Give the extent of all uninfected red blood cells.
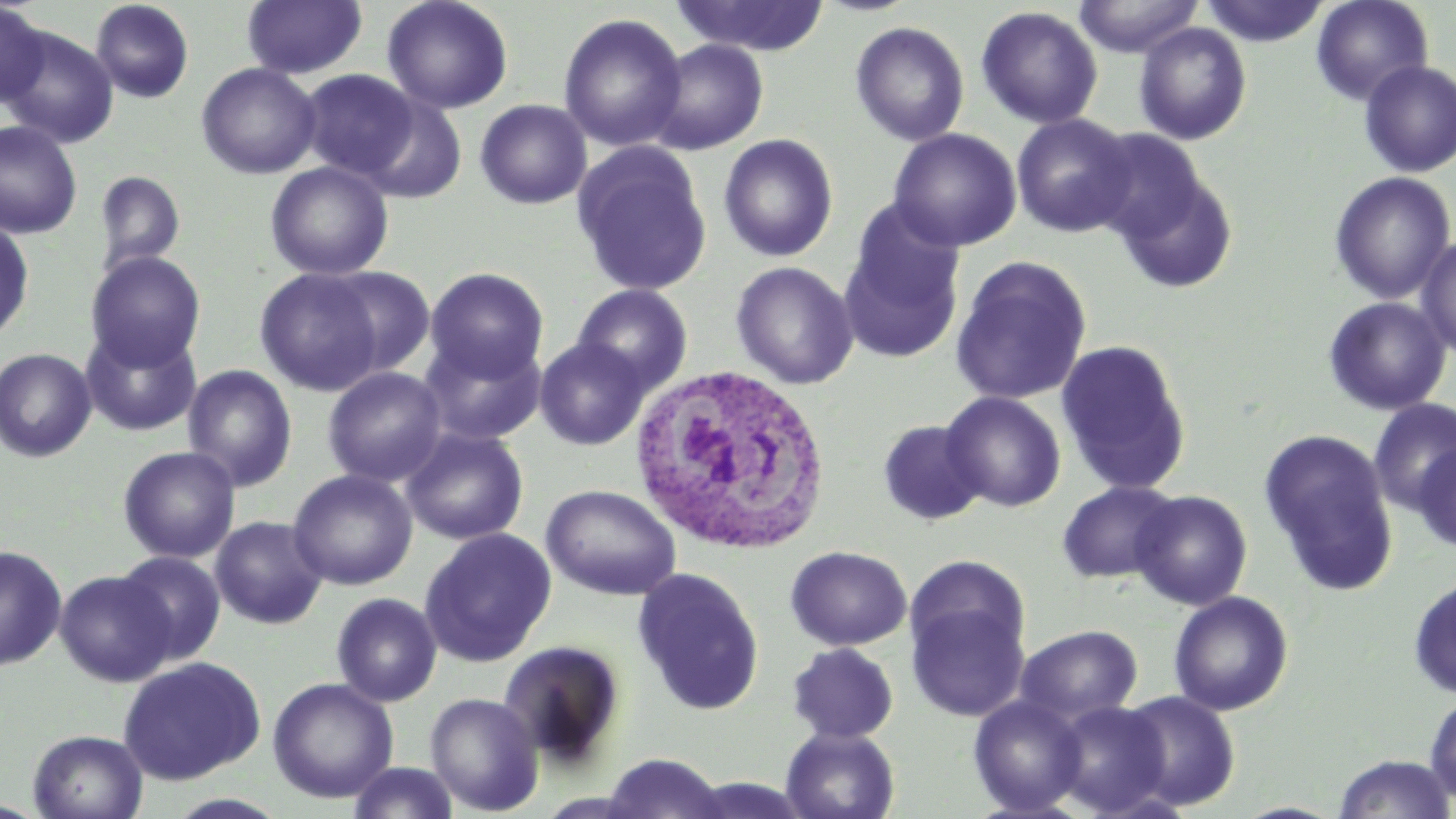

Approximate bounding boxes as named x1/y1/x2/y2 corners in pixels.
Uninfected red blood cells: (x1=90, y1=0, x2=194, y2=103), (x1=241, y1=0, x2=367, y2=80), (x1=382, y1=0, x2=514, y2=114), (x1=669, y1=0, x2=831, y2=56), (x1=1072, y1=0, x2=1204, y2=58), (x1=1199, y1=0, x2=1331, y2=47), (x1=1310, y1=0, x2=1434, y2=106), (x1=0, y1=1, x2=49, y2=108), (x1=975, y1=6, x2=1103, y2=129), (x1=558, y1=13, x2=687, y2=151), (x1=849, y1=21, x2=970, y2=146), (x1=1133, y1=22, x2=1252, y2=145), (x1=1, y1=26, x2=119, y2=148), (x1=648, y1=38, x2=770, y2=155), (x1=1358, y1=60, x2=1456, y2=178), (x1=196, y1=62, x2=322, y2=179), (x1=299, y1=69, x2=419, y2=179), (x1=356, y1=94, x2=468, y2=204), (x1=475, y1=99, x2=592, y2=209), (x1=1011, y1=113, x2=1136, y2=237), (x1=0, y1=120, x2=82, y2=239), (x1=1085, y1=127, x2=1212, y2=247), (x1=888, y1=128, x2=1022, y2=252), (x1=719, y1=133, x2=838, y2=262), (x1=572, y1=142, x2=713, y2=298), (x1=265, y1=161, x2=394, y2=281), (x1=1112, y1=166, x2=1239, y2=294), (x1=94, y1=171, x2=186, y2=275), (x1=1329, y1=171, x2=1456, y2=305), (x1=837, y1=211, x2=965, y2=364), (x1=0, y1=219, x2=34, y2=343), (x1=1415, y1=234, x2=1456, y2=360), (x1=85, y1=251, x2=206, y2=370), (x1=950, y1=256, x2=1092, y2=405), (x1=731, y1=261, x2=859, y2=389), (x1=321, y1=266, x2=437, y2=377), (x1=424, y1=267, x2=548, y2=382), (x1=255, y1=268, x2=385, y2=396), (x1=572, y1=284, x2=693, y2=395), (x1=1322, y1=297, x2=1451, y2=415), (x1=80, y1=326, x2=201, y2=436), (x1=420, y1=334, x2=546, y2=445), (x1=534, y1=337, x2=651, y2=450), (x1=1056, y1=339, x2=1192, y2=495), (x1=0, y1=348, x2=97, y2=462), (x1=182, y1=364, x2=298, y2=491), (x1=322, y1=367, x2=447, y2=487), (x1=940, y1=391, x2=1066, y2=512), (x1=1368, y1=399, x2=1456, y2=515), (x1=878, y1=420, x2=987, y2=526), (x1=400, y1=427, x2=529, y2=545), (x1=1258, y1=429, x2=1399, y2=596), (x1=1413, y1=441, x2=1456, y2=552), (x1=118, y1=445, x2=240, y2=563), (x1=287, y1=469, x2=418, y2=591), (x1=1056, y1=481, x2=1183, y2=584), (x1=541, y1=484, x2=682, y2=600), (x1=1130, y1=490, x2=1252, y2=610), (x1=210, y1=516, x2=328, y2=630), (x1=419, y1=528, x2=557, y2=667), (x1=0, y1=544, x2=67, y2=671), (x1=785, y1=545, x2=912, y2=651), (x1=115, y1=551, x2=226, y2=663), (x1=904, y1=554, x2=1032, y2=665), (x1=631, y1=567, x2=765, y2=715), (x1=54, y1=569, x2=176, y2=686), (x1=1408, y1=573, x2=1456, y2=699), (x1=1168, y1=591, x2=1294, y2=716), (x1=331, y1=592, x2=442, y2=707), (x1=907, y1=599, x2=1030, y2=721), (x1=1015, y1=625, x2=1143, y2=725), (x1=497, y1=640, x2=626, y2=769), (x1=787, y1=643, x2=899, y2=744), (x1=117, y1=656, x2=266, y2=786), (x1=267, y1=677, x2=399, y2=803), (x1=1423, y1=690, x2=1456, y2=806), (x1=1118, y1=691, x2=1241, y2=811), (x1=425, y1=692, x2=544, y2=816), (x1=968, y1=695, x2=1089, y2=816), (x1=1048, y1=700, x2=1172, y2=817), (x1=781, y1=727, x2=900, y2=819), (x1=28, y1=730, x2=148, y2=818), (x1=600, y1=753, x2=729, y2=818), (x1=1332, y1=754, x2=1456, y2=818), (x1=347, y1=762, x2=460, y2=819), (x1=164, y1=793, x2=292, y2=818).

White blood cell locations: (x1=627, y1=365, x2=830, y2=554). Slide-level diagnosis: negative for blood parasites. Image is 1456×819 pixels. Optical microscopy. Single field of view. May-Grünwald-Giemsa-stained preparation. 1000x magnification. Thin blood smear.